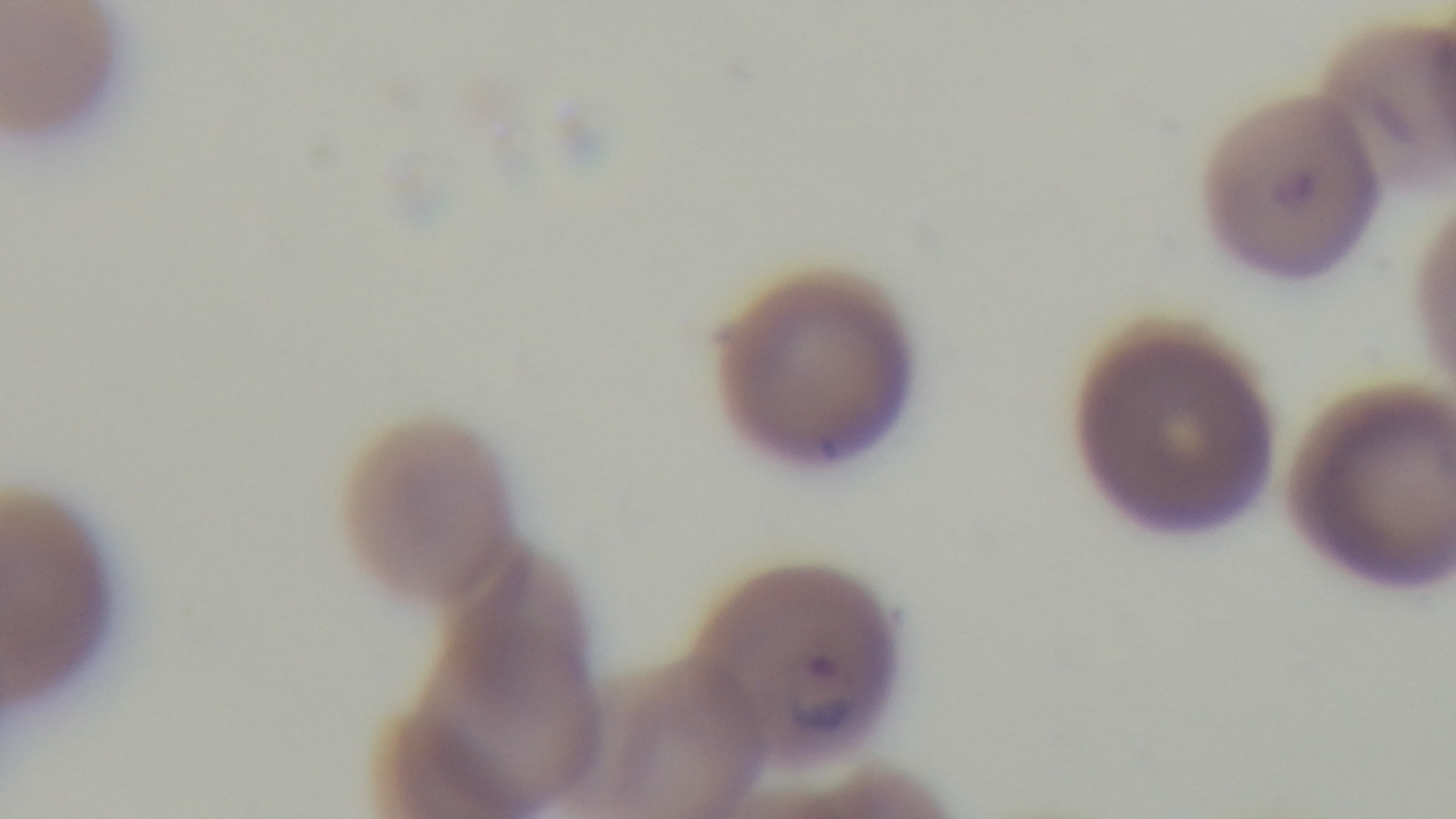 100x oil-immersion objective. Preparation: thin smear. Captured with a mounted 4K digital camera. Light microscopy. Malaria status: positive. Single field of view. Giemsa-stained.